Comment on the morphology of the erythrocytes.
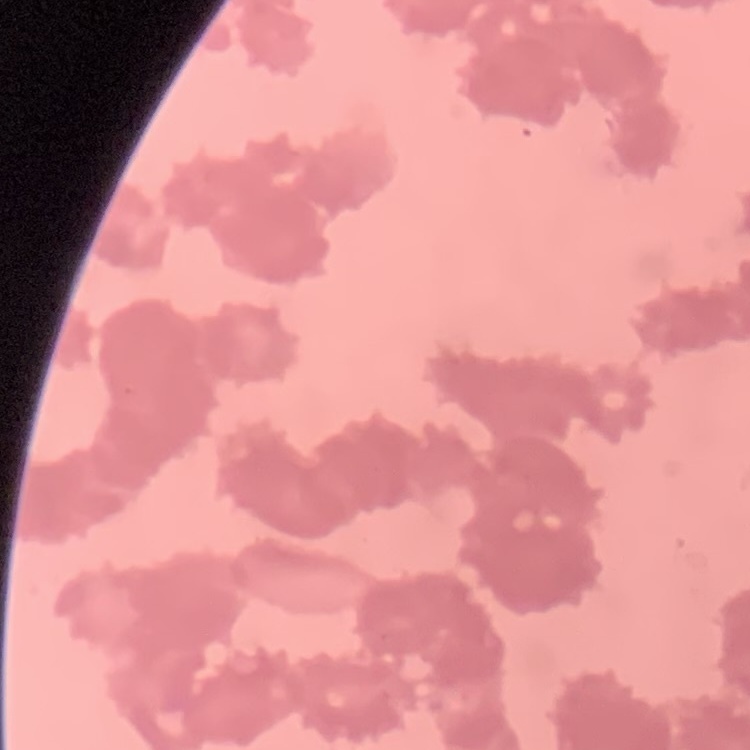

They show rouleaux formation.

Summary:
  - Preparation: thin peripheral smear
  - Stain: Field's or Giemsa
  - Image type: one tile cut from a larger photomicrograph